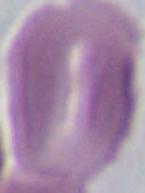

Summary:
  - Modality: photomicrograph
  - Magnification: 1000x
  - Identification: erythrocyte